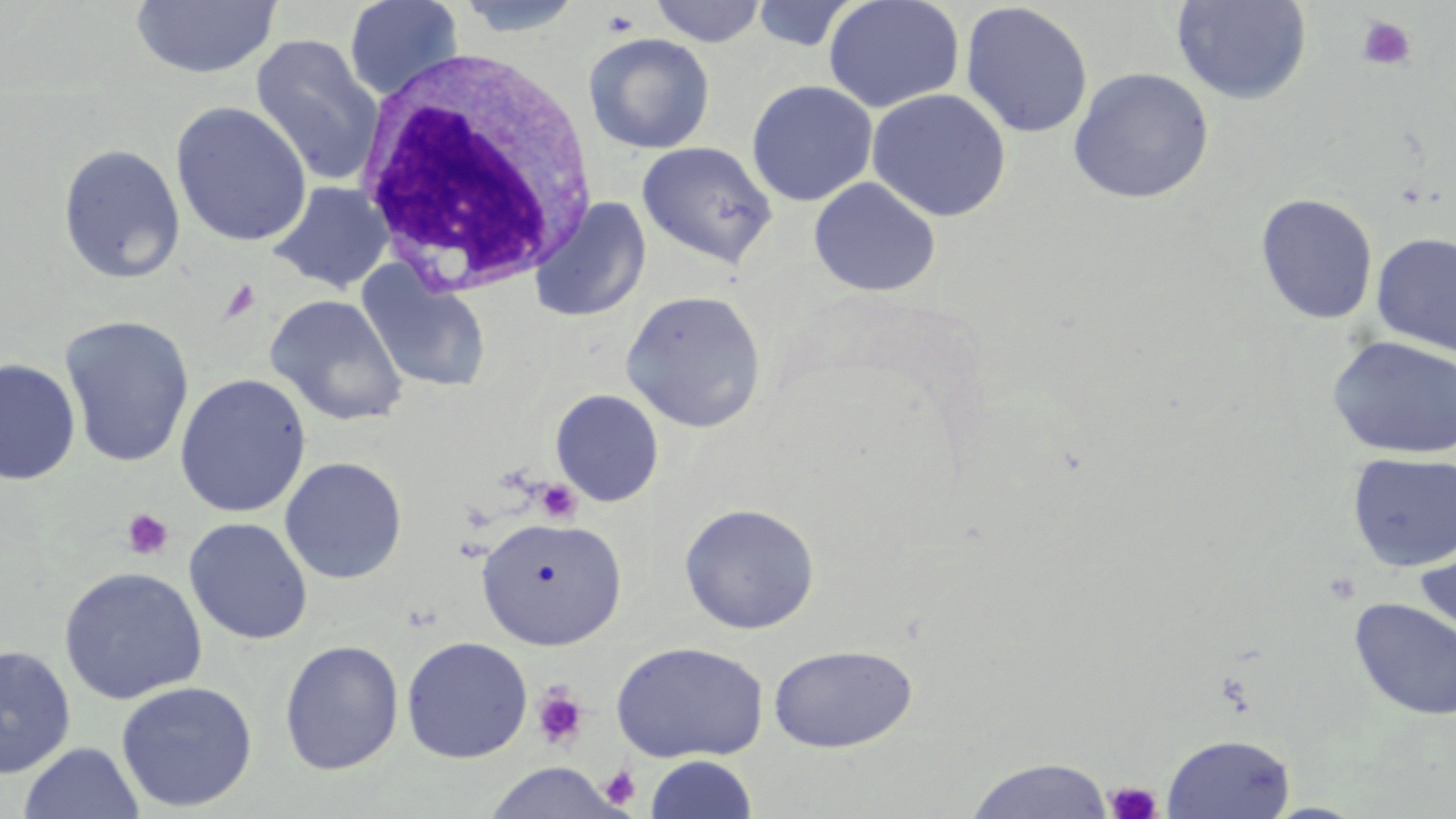
Approximate bounding boxes as (x1, y1, x2, y2) in pixels. Uninfected red blood cell locations: (343, 0, 465, 100), (451, 0, 590, 37), (648, 0, 768, 47), (823, 0, 965, 114), (1171, 0, 1312, 105), (129, 1, 281, 79), (750, 1, 861, 52), (959, 2, 1093, 138), (584, 32, 716, 154), (249, 34, 384, 186), (1068, 67, 1215, 204), (746, 80, 878, 206), (867, 88, 1012, 221), (170, 102, 312, 246), (637, 141, 778, 268), (57, 143, 186, 284), (808, 177, 942, 297), (268, 181, 393, 294), (1255, 193, 1379, 325), (530, 197, 651, 323), (1371, 232, 1456, 356), (358, 264, 492, 394), (621, 289, 767, 433), (265, 294, 408, 427), (59, 315, 195, 468), (1326, 334, 1456, 461), (0, 358, 81, 486), (175, 373, 311, 517), (549, 389, 664, 507), (1347, 452, 1456, 573), (280, 457, 407, 584), (679, 502, 820, 634), (476, 516, 627, 650), (183, 517, 313, 645), (1414, 539, 1456, 649), (59, 566, 207, 704), (1349, 597, 1456, 721), (401, 636, 533, 763), (280, 639, 404, 775), (611, 640, 769, 763), (768, 643, 918, 752), (0, 644, 76, 778), (116, 680, 257, 812), (1161, 733, 1296, 818), (18, 742, 144, 819), (645, 755, 758, 818), (965, 758, 1114, 819), (482, 763, 624, 819). White blood cell locations: (352, 45, 603, 300). Platelet locations: (600, 7, 641, 38), (1355, 15, 1417, 71), (219, 280, 261, 323), (535, 479, 582, 524), (121, 509, 174, 560), (532, 684, 590, 751), (598, 765, 641, 809), (1105, 780, 1162, 819). Slide-level diagnosis: no evidence of blood parasites. Image is 1456×819 pixels. One field of a larger specimen. Captured at 1000x magnification. May-Grünwald-Giemsa stain. Thin blood film. Light microscopy.